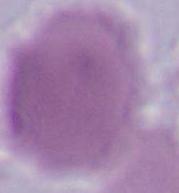 Micrograph. A red blood cell is shown. Captured at 1000x magnification.